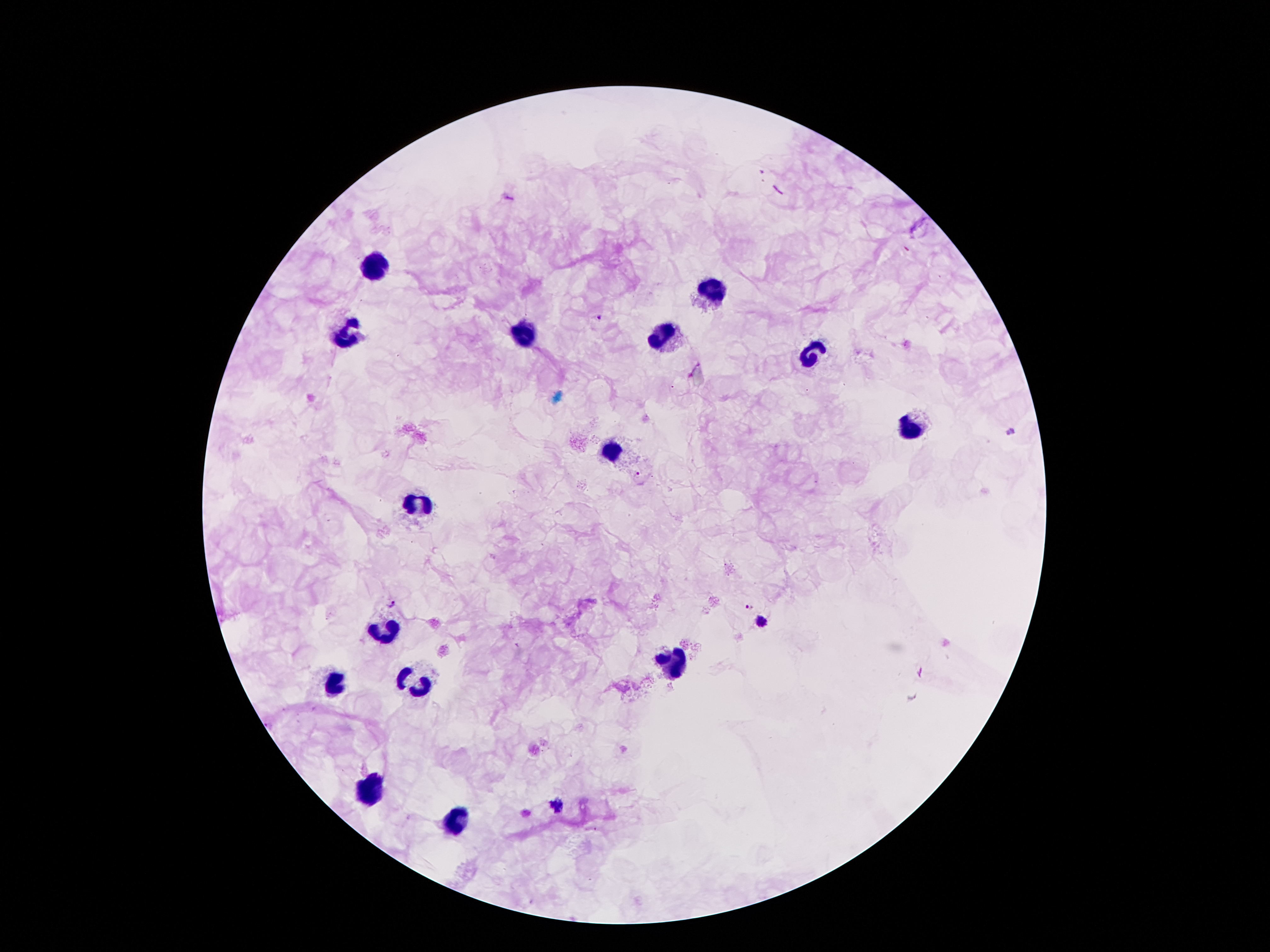
Approximate centers as {x, y} in pixels. Plasmodium parasite locations: {598, 316}, {1010, 432}, {636, 472}, {390, 602}, {750, 607}, {760, 621}, {556, 805}. Leukocyte locations: {372, 267}, {713, 290}, {347, 332}, {668, 334}, {524, 338}, {815, 350}, {916, 426}, {612, 451}, {419, 502}, {385, 628}, {668, 665}, {332, 682}, {414, 684}, {370, 787}, {454, 821}. Patient malaria status: positive for Plasmodium falciparum. Giemsa-stained preparation. Thick peripheral-blood smear. 100x magnification. Image is 1270×952 pixels. Single field of view. Smartphone photograph taken through the microscope eyepiece.